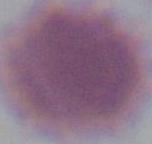

identification = erythrocyte
magnification = 1000x
modality = photomicrograph